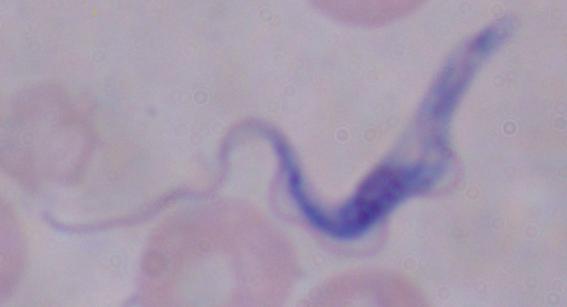

Summary:
  - Magnification: 1000x
  - Identification: trypanosome
  - Modality: micrograph